Outline white blood cells.
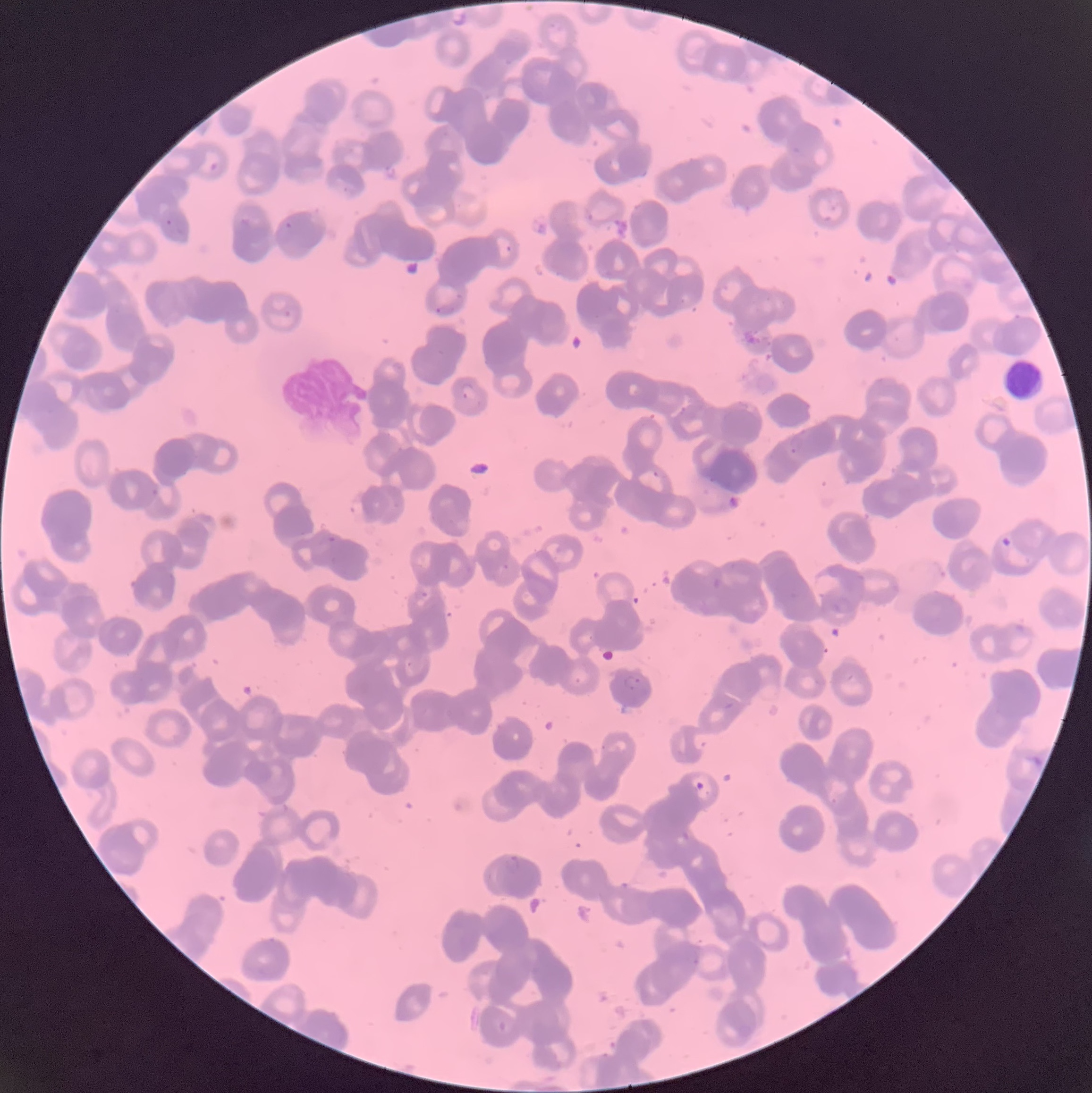

Approximate bounding boxes as named x1/y1/x2/y2 corners in pixels.
White blood cells: (x1=1004, y1=358, x2=1043, y2=400).

Plasmodium parasite locations: (x1=208, y1=160, x2=220, y2=173), (x1=164, y1=218, x2=174, y2=228), (x1=276, y1=220, x2=298, y2=246), (x1=435, y1=305, x2=453, y2=316), (x1=461, y1=382, x2=475, y2=401), (x1=789, y1=434, x2=803, y2=454), (x1=319, y1=534, x2=338, y2=546), (x1=415, y1=589, x2=429, y2=599), (x1=623, y1=673, x2=640, y2=691), (x1=502, y1=853, x2=522, y2=875). Image is 1092×1093 pixels. Thin blood smear. Optical microscopy. The red blood cells show rouleaux formation.